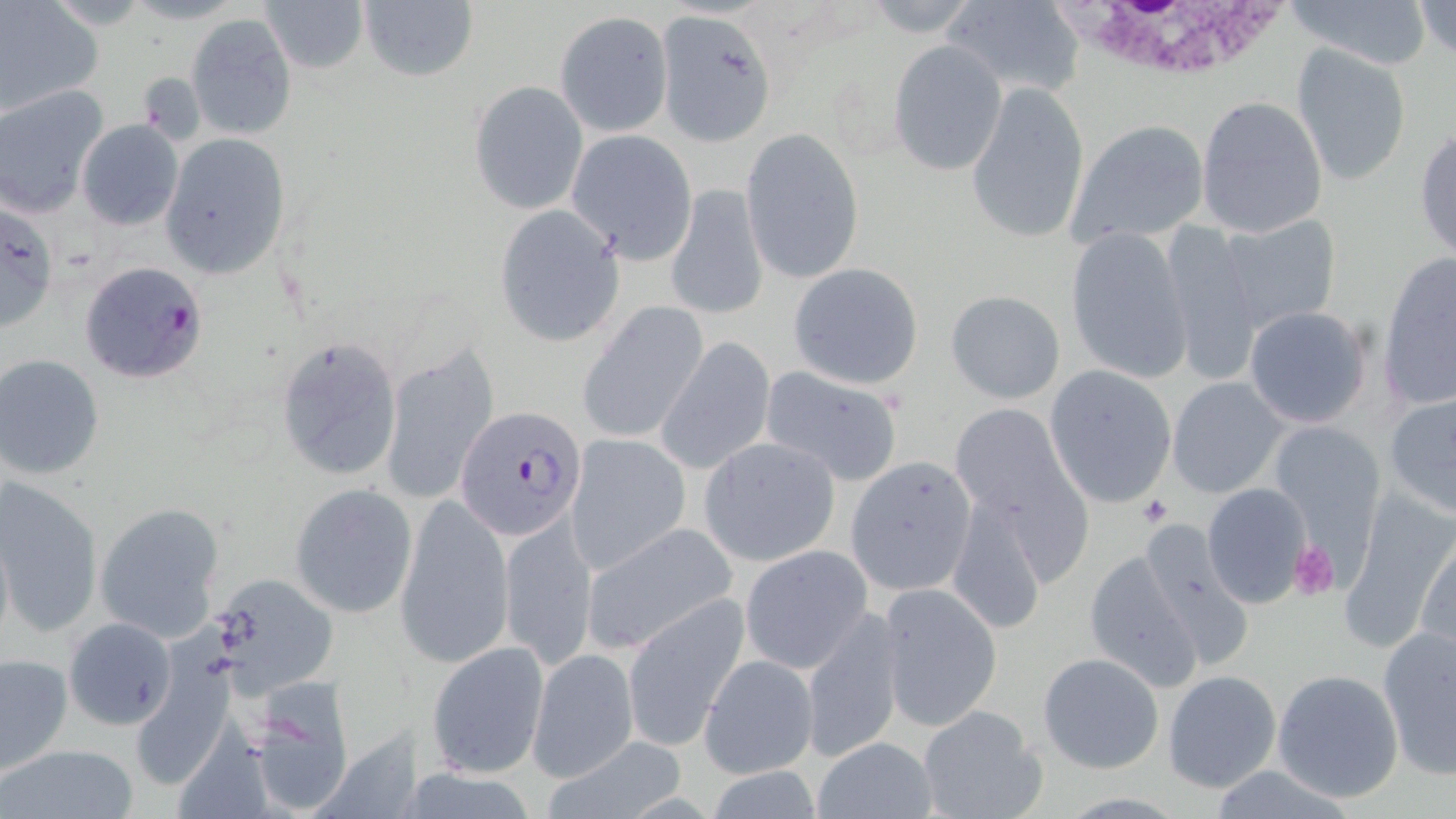 Approximate bounding boxes as named x1/y1/x2/y2 corners in pixels. Platelet locations: (x1=1140, y1=496, x2=1174, y2=526), (x1=1289, y1=540, x2=1339, y2=599). White blood cell locations: (x1=1056, y1=1, x2=1303, y2=85). Plasmodium falciparum-infected red blood cell locations: (x1=77, y1=261, x2=207, y2=384), (x1=455, y1=406, x2=586, y2=540). Uninfected red blood cell locations: (x1=260, y1=0, x2=367, y2=73), (x1=940, y1=0, x2=1086, y2=95), (x1=1290, y1=0, x2=1430, y2=71), (x1=357, y1=1, x2=479, y2=83), (x1=1413, y1=1, x2=1456, y2=59), (x1=0, y1=2, x2=102, y2=116), (x1=654, y1=8, x2=776, y2=145), (x1=556, y1=11, x2=671, y2=137), (x1=186, y1=13, x2=297, y2=138), (x1=888, y1=38, x2=1007, y2=176), (x1=1290, y1=44, x2=1413, y2=188), (x1=469, y1=80, x2=588, y2=215), (x1=966, y1=81, x2=1089, y2=245), (x1=0, y1=86, x2=107, y2=216), (x1=1196, y1=95, x2=1328, y2=239), (x1=1065, y1=119, x2=1211, y2=246), (x1=76, y1=120, x2=183, y2=230), (x1=1414, y1=126, x2=1456, y2=264), (x1=742, y1=127, x2=865, y2=285), (x1=566, y1=128, x2=697, y2=262), (x1=159, y1=133, x2=291, y2=279), (x1=665, y1=181, x2=769, y2=321), (x1=494, y1=206, x2=624, y2=346), (x1=1212, y1=213, x2=1342, y2=334), (x1=1159, y1=221, x2=1262, y2=385), (x1=1064, y1=227, x2=1193, y2=385), (x1=1378, y1=253, x2=1456, y2=411), (x1=787, y1=261, x2=924, y2=390), (x1=944, y1=289, x2=1067, y2=405), (x1=578, y1=302, x2=709, y2=443), (x1=1243, y1=304, x2=1374, y2=428), (x1=274, y1=334, x2=403, y2=483), (x1=658, y1=336, x2=777, y2=475), (x1=379, y1=342, x2=499, y2=506), (x1=0, y1=355, x2=105, y2=479), (x1=760, y1=366, x2=905, y2=486), (x1=1044, y1=366, x2=1177, y2=508), (x1=1165, y1=375, x2=1290, y2=498), (x1=1383, y1=392, x2=1456, y2=518), (x1=947, y1=400, x2=1084, y2=534), (x1=1266, y1=421, x2=1386, y2=556), (x1=565, y1=434, x2=690, y2=576), (x1=699, y1=437, x2=840, y2=566), (x1=851, y1=450, x2=982, y2=638), (x1=0, y1=475, x2=103, y2=639), (x1=291, y1=484, x2=419, y2=618), (x1=1201, y1=484, x2=1313, y2=609), (x1=946, y1=489, x2=1048, y2=637), (x1=1339, y1=491, x2=1455, y2=648), (x1=397, y1=496, x2=513, y2=667), (x1=95, y1=501, x2=225, y2=643), (x1=501, y1=514, x2=596, y2=668), (x1=1134, y1=516, x2=1254, y2=663), (x1=579, y1=520, x2=738, y2=656), (x1=0, y1=526, x2=13, y2=648), (x1=1414, y1=529, x2=1455, y2=663), (x1=739, y1=545, x2=873, y2=674), (x1=1084, y1=548, x2=1203, y2=691), (x1=206, y1=574, x2=338, y2=697), (x1=879, y1=582, x2=1003, y2=730), (x1=623, y1=595, x2=751, y2=751), (x1=802, y1=607, x2=904, y2=763), (x1=64, y1=617, x2=179, y2=731), (x1=1378, y1=625, x2=1456, y2=777), (x1=425, y1=641, x2=550, y2=778), (x1=527, y1=647, x2=638, y2=781), (x1=1035, y1=651, x2=1165, y2=774), (x1=129, y1=652, x2=237, y2=789), (x1=1, y1=653, x2=73, y2=777), (x1=699, y1=653, x2=817, y2=779), (x1=1270, y1=667, x2=1404, y2=801), (x1=1162, y1=670, x2=1283, y2=793), (x1=243, y1=683, x2=358, y2=814), (x1=916, y1=704, x2=1048, y2=819), (x1=812, y1=735, x2=941, y2=819), (x1=545, y1=739, x2=688, y2=819), (x1=1, y1=742, x2=142, y2=819). Slide-level diagnosis: Plasmodium falciparum. Thin blood smear. May-Grünwald-Giemsa stain. One field of a larger specimen. Light microscopy. Image is 1456×819 pixels. Captured at 1000x magnification.